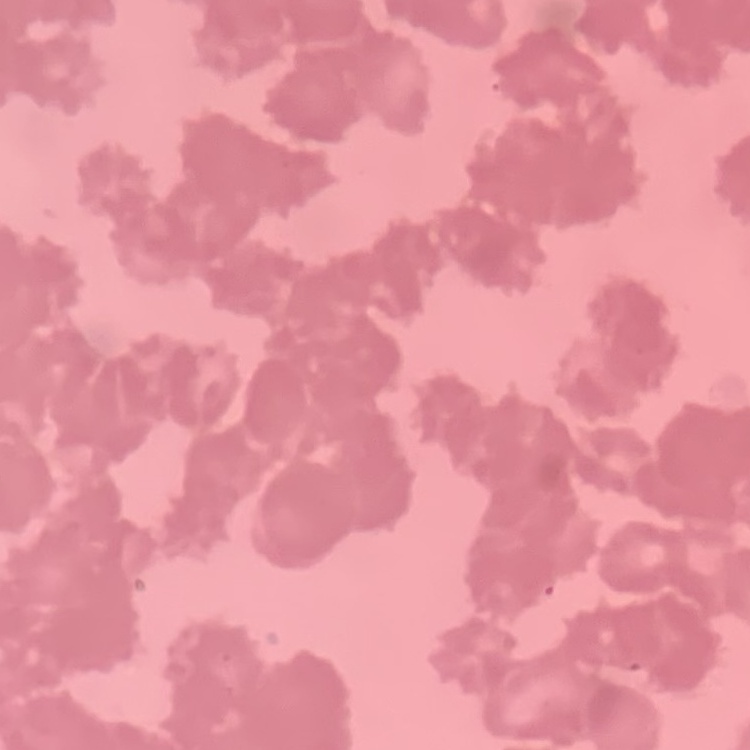

{
  "red_blood_cell_morphology": "rouleaux formation",
  "preparation": "thin blood smear",
  "stain": "Field's or Giemsa",
  "image_type": "square crop of a larger photomicrograph"
}